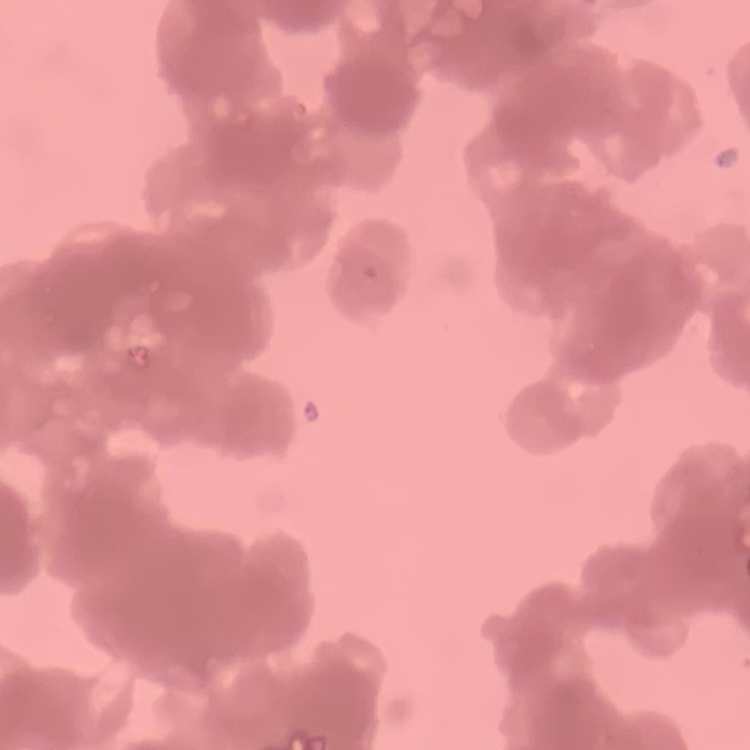
erythrocyte morphology = rouleaux formation
image type = square crop of a larger photomicrograph
stain = Field's or Giemsa
preparation = thin peripheral smear